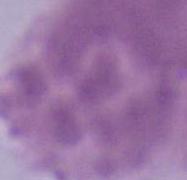

Summary:
  - Magnification: 1000x
  - Identification: erythrocyte
  - Modality: photomicrograph